Assess this cell for malaria.
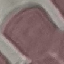

It is uninfected.

Summary:
  - Capture: smartphone through the microscope eyepiece
  - Stain: Giemsa
  - Image type: automatically extracted cell patch, resized to 64 × 64 pixels
  - Preparation: thin smear